Assess this cell for malaria.
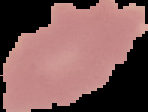

Uninfected.

{
  "image_type": "segmented cell region with the area outside set to black",
  "preparation": "thin blood film",
  "image_size": "148×112 pixels"
}